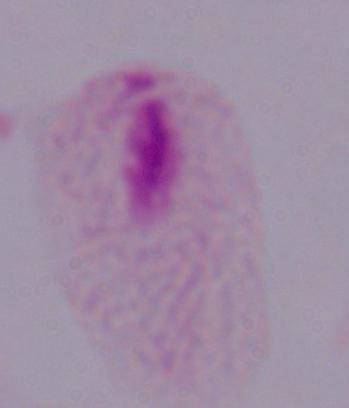

Summary:
  - Identification: trichomonad
  - Modality: micrograph
  - Magnification: 1000x